Point out each Plasmodium parasite and each leukocyte.
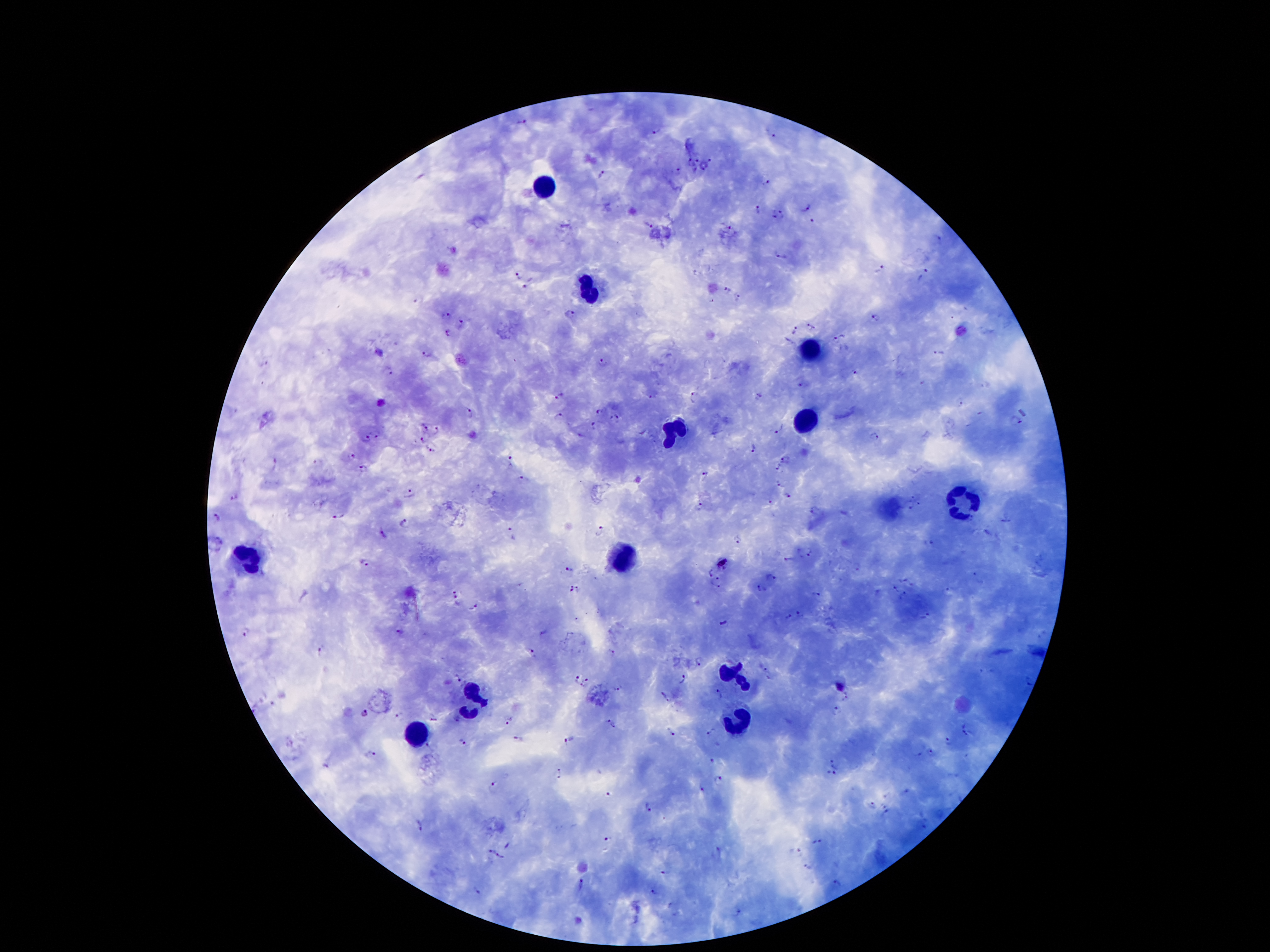
Approximate centers as (x, y) in pixels.
Plasmodium parasites: (523, 121), (656, 129), (774, 135), (712, 157), (696, 160), (690, 163), (704, 166), (680, 169), (601, 174), (767, 182), (806, 207), (758, 211), (773, 214), (783, 214), (813, 218), (650, 225), (729, 226), (937, 238), (781, 257), (881, 268), (517, 274), (922, 278), (528, 282), (726, 289), (737, 295), (420, 301), (570, 313), (446, 314), (876, 318), (461, 322), (810, 328), (795, 329), (447, 332), (840, 339), (788, 340), (941, 351), (380, 352), (427, 352), (603, 360), (262, 363), (391, 371), (855, 373), (801, 385), (559, 394), (695, 396), (652, 397), (759, 397), (961, 402), (598, 411), (469, 412), (559, 417), (618, 418), (424, 425), (595, 425), (779, 428), (438, 432), (377, 434), (874, 436), (423, 439), (366, 440), (753, 448), (430, 450), (352, 458), (786, 459), (511, 460), (317, 462), (275, 463), (779, 467), (364, 470), (705, 474), (521, 477), (779, 482), (409, 491), (233, 495), (787, 495), (914, 496), (771, 502), (921, 502), (910, 507), (699, 509), (812, 509), (341, 516), (217, 518), (1005, 520), (406, 521), (600, 528), (987, 529), (512, 534), (382, 535), (737, 540), (928, 542), (811, 551), (789, 559), (363, 564), (859, 568), (568, 570), (711, 572), (976, 573), (720, 577), (771, 579), (714, 585), (760, 587), (570, 588), (578, 589), (894, 589), (950, 590), (456, 596), (814, 596), (473, 605), (799, 613), (925, 617), (788, 618), (723, 623), (399, 631), (247, 633), (321, 648), (611, 651), (532, 652), (698, 661), (766, 669), (459, 677), (575, 680), (683, 680), (1030, 680), (585, 682), (615, 690), (719, 692), (665, 697), (846, 697), (838, 711), (364, 712), (398, 716), (432, 719), (458, 719), (511, 720), (608, 720), (614, 726), (671, 731), (712, 731), (964, 731), (519, 738), (567, 738), (462, 740), (948, 741), (429, 744), (371, 750), (930, 753), (712, 761), (835, 764), (326, 767), (560, 772), (829, 775), (719, 779), (493, 784), (703, 789), (606, 796), (872, 804), (648, 806), (887, 810), (417, 823), (609, 839), (818, 840), (509, 845), (717, 848), (488, 849), (501, 855), (808, 867), (665, 872), (837, 883), (583, 885), (479, 891), (653, 891), (738, 912).
Leukocytes: (542, 183), (590, 287), (812, 351), (807, 422), (672, 429), (964, 502), (252, 559), (621, 559), (736, 676), (473, 694), (736, 721), (416, 734).

Summary:
  - Preparation: thick blood film
  - Magnification: 100x
  - Patient malaria status: positive for Plasmodium falciparum
  - Field of view: one from this slide
  - Image size: 1270×952 pixels
  - Capture: smartphone through the microscope eyepiece
  - Stain: Giemsa